Classify this cell by malaria status.
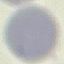

Uninfected.

Automatically extracted cell patch, resized to 64 × 64 pixels. Giemsa stain. Thin blood smear. Acquired by smartphone through the microscope eyepiece.